Report the malaria status of this cell.
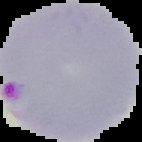

It is parasitized.

Summary:
  - Image size: 142×142 pixels
  - Image type: segmented cell region with the area outside set to black
  - Preparation: thin blood smear